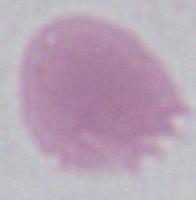
Summary:
  - Magnification: 1000x
  - Modality: photomicrograph
  - Identification: erythrocyte